Name the parasite shown.
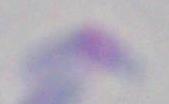

Toxoplasma gondii.

Summary:
  - Modality: micrograph
  - Magnification: 1000x